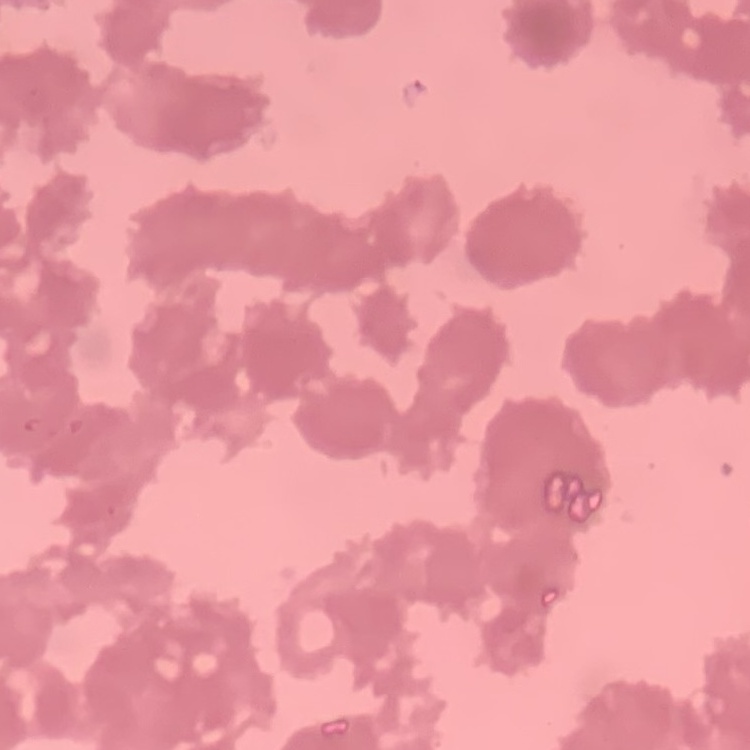 The red blood cells show rouleaux formation. Stained with either Field's or Giemsa. Thin blood smear. One tile cut from a larger photomicrograph.